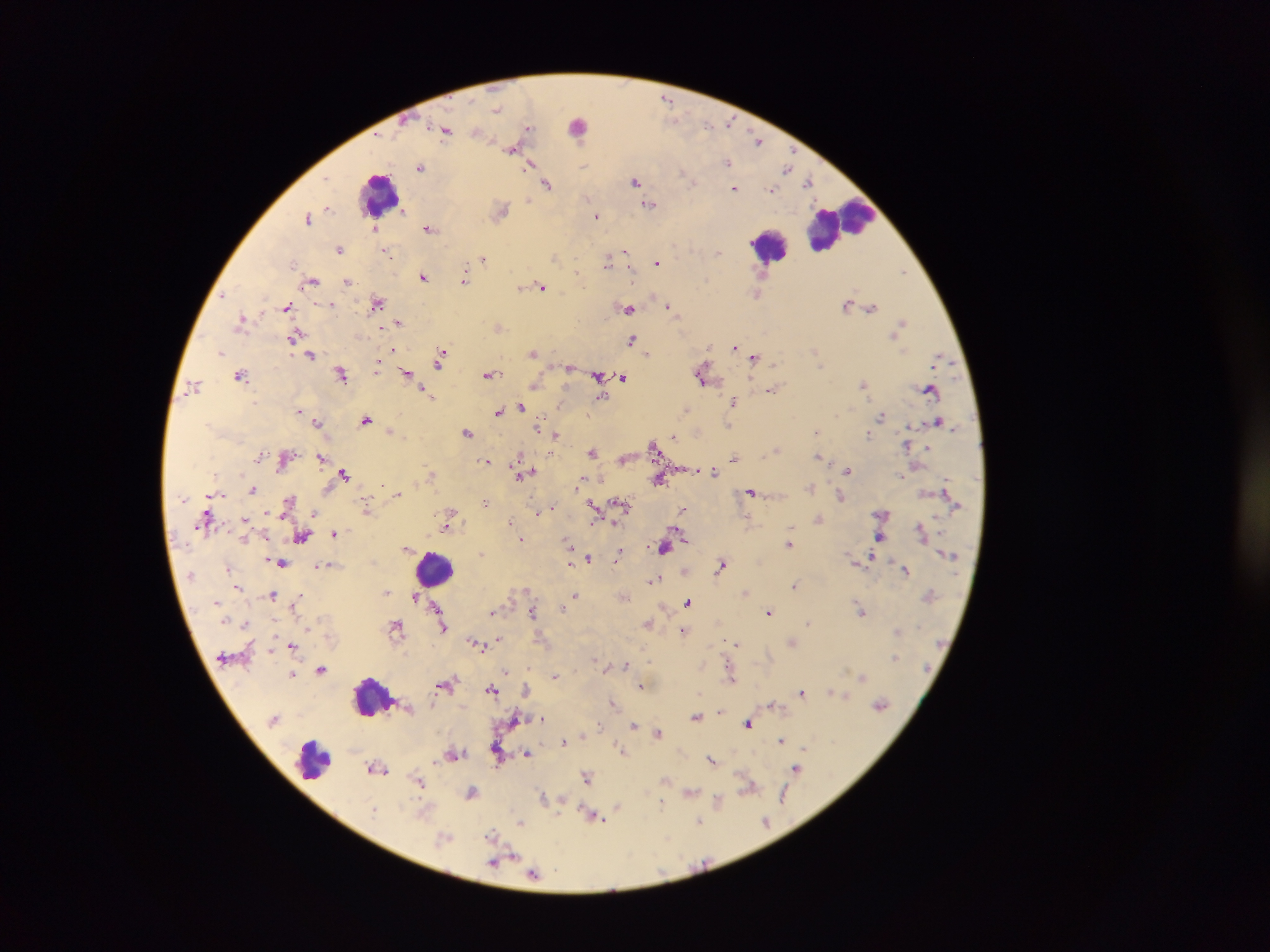
capture = mobile-phone photograph through a microscope
field of view = single
leukocyte locations = approximate centers as [x, y] in pixels: [579, 124], [379, 193], [839, 225], [769, 245], [434, 568], [371, 697], [312, 760]
country = Ghana
image size = 1270×952 pixels
preparation = thick blood film
Plasmodium parasite locations = approximate centers as [x, y] in pixels: [667, 100], [497, 110], [730, 123], [708, 125], [527, 128], [445, 131], [478, 131], [757, 139], [512, 150], [728, 162], [532, 164], [420, 167], [786, 168], [683, 172], [636, 181], [808, 181], [692, 182], [547, 184], [734, 188], [772, 190], [528, 199], [649, 205], [328, 207], [404, 211], [502, 211], [596, 215], [308, 218], [374, 227], [429, 228], [340, 249], [718, 251], [625, 252], [387, 253], [554, 257], [483, 259], [608, 261], [657, 263], [293, 265], [903, 271], [578, 273], [423, 276], [312, 281], [464, 281], [348, 282], [520, 287], [542, 287], [757, 293], [223, 296], [377, 303], [331, 305], [669, 305], [847, 305], [286, 307], [871, 307], [628, 308], [242, 320], [398, 322], [902, 323], [499, 327], [294, 336], [632, 339], [709, 347], [735, 347], [221, 352], [534, 352], [647, 353], [311, 355], [754, 357], [441, 358], [378, 359], [377, 366], [569, 369], [407, 373], [341, 374], [240, 375], [489, 375], [599, 376], [701, 376], [623, 377], [863, 383], [195, 385], [535, 385], [930, 389], [772, 390], [426, 393], [431, 396], [601, 398], [734, 402], [522, 407], [687, 410], [299, 411], [499, 411], [881, 416], [366, 420], [938, 421], [317, 422], [539, 424], [729, 424], [390, 431], [817, 431], [468, 433], [556, 435], [868, 435], [674, 436], [653, 447], [928, 447], [776, 450], [593, 452], [819, 456], [320, 457], [734, 458], [518, 459], [486, 460], [848, 471], [524, 472], [344, 473], [714, 473], [902, 476], [660, 479], [580, 483], [810, 488], [253, 489], [751, 492], [397, 493], [841, 497], [290, 500], [485, 503], [622, 503], [366, 507], [594, 508], [549, 510], [682, 510], [538, 512], [314, 513], [452, 513], [245, 519], [818, 519], [511, 523], [447, 526], [790, 528], [678, 532], [334, 533], [303, 537], [879, 537], [521, 540], [789, 543], [570, 544], [408, 548], [664, 548], [619, 552], [481, 554], [589, 558], [282, 562], [569, 562], [722, 564], [319, 566], [228, 568], [906, 570], [653, 580], [794, 585], [237, 588], [386, 592], [745, 592], [273, 595], [575, 596], [414, 597], [299, 598], [296, 602], [689, 602], [437, 606], [563, 607], [533, 611], [861, 611], [769, 612], [493, 613], [648, 623], [808, 623], [246, 624], [397, 626], [444, 628], [683, 630], [897, 631], [498, 639], [792, 642], [736, 643], [476, 644], [292, 646], [895, 657], [650, 659], [596, 660], [626, 665], [321, 670], [507, 672], [293, 675], [555, 676], [862, 676], [731, 678], [445, 684], [641, 685], [492, 689], [526, 689], [802, 692], [833, 692], [843, 695], [613, 703], [880, 704], [720, 711], [696, 717], [542, 719], [634, 724], [747, 724], [600, 726], [658, 732], [781, 740], [563, 742], [805, 748], [621, 750], [453, 753], [527, 753], [711, 759], [378, 769], [796, 769], [587, 776], [418, 781], [749, 787], [471, 792], [690, 792], [784, 796], [542, 798], [718, 800], [661, 802], [617, 806], [373, 809], [594, 816], [699, 821], [766, 822], [521, 823], [492, 833], [445, 837], [511, 855], [497, 861], [533, 873]